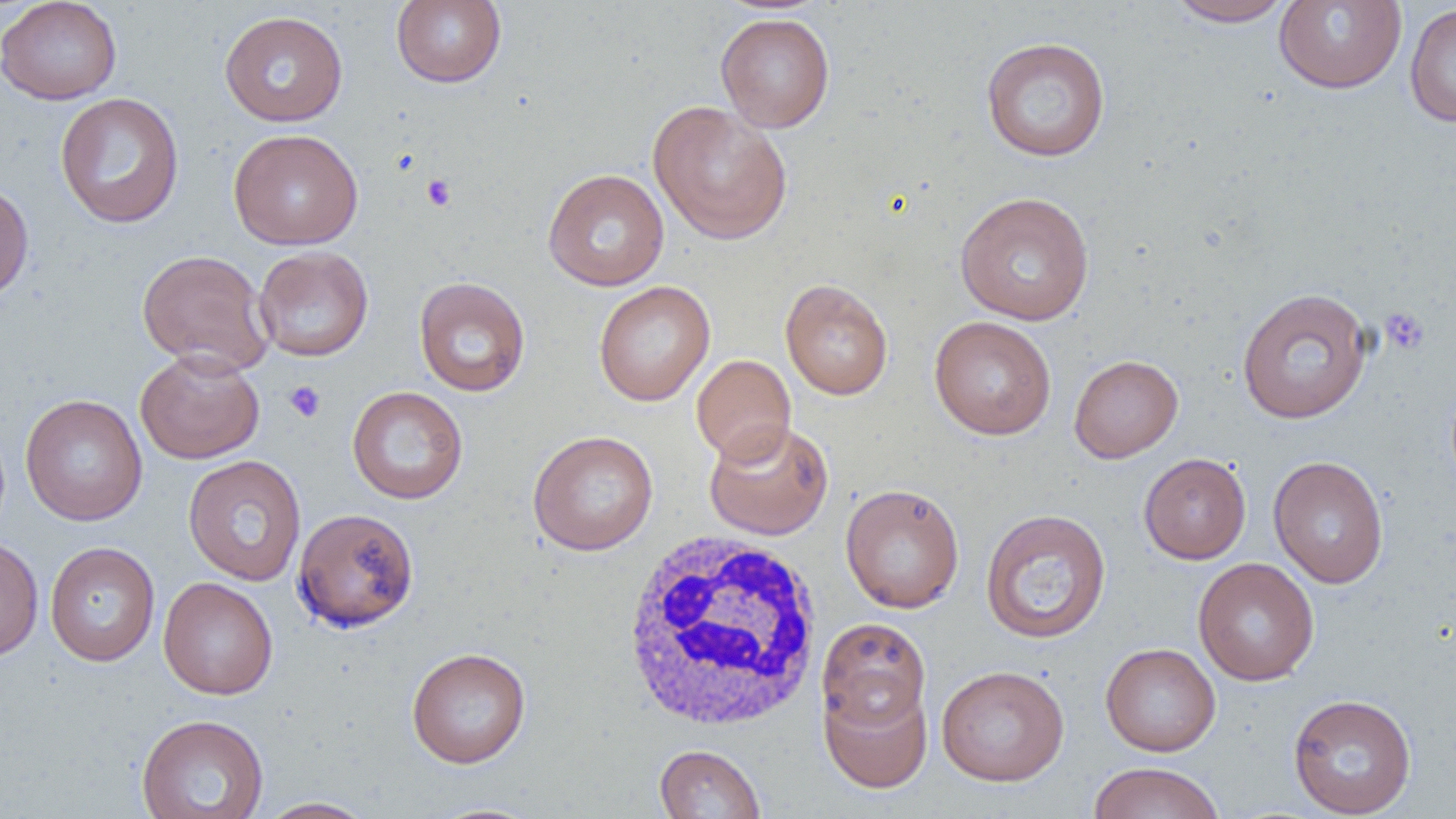
{
  "slide_level_diagnosis": "no evidence of blood parasites",
  "magnification": "1000x",
  "white_blood_cell_locations": "approximate bounding boxes as [x1, y1, x2, y2] in pixels: [618, 531, 824, 733]",
  "field_of_view": "one of a larger specimen",
  "uninfected_red_blood_cell_locations": "approximate bounding boxes as [x1, y1, x2, y2] in pixels: [0, 0, 122, 105], [391, 0, 507, 88], [1166, 0, 1295, 27], [1273, 0, 1407, 94], [1404, 4, 1456, 127], [219, 10, 349, 127], [715, 12, 836, 133], [980, 36, 1111, 162], [54, 92, 185, 228], [647, 101, 794, 246], [228, 128, 364, 251], [542, 168, 670, 291], [0, 179, 34, 306], [954, 191, 1095, 325], [252, 246, 373, 362], [136, 249, 274, 375], [414, 276, 530, 397], [779, 278, 894, 400], [593, 281, 715, 406], [1236, 287, 1373, 424], [929, 315, 1057, 440], [134, 348, 265, 464], [691, 354, 796, 464], [1069, 354, 1183, 463], [346, 386, 469, 504], [20, 394, 148, 526], [704, 419, 834, 541], [527, 430, 659, 556], [1139, 452, 1252, 564], [183, 454, 307, 586], [1268, 455, 1389, 588], [840, 483, 965, 613], [293, 508, 419, 633], [979, 508, 1112, 644], [0, 535, 44, 661], [45, 541, 161, 666], [1193, 557, 1320, 686], [158, 576, 279, 699], [816, 618, 931, 731], [1100, 642, 1221, 756], [406, 647, 531, 769], [936, 664, 1070, 786], [819, 678, 933, 793], [1288, 693, 1417, 817], [136, 713, 270, 819], [653, 744, 766, 818], [1086, 761, 1226, 819], [255, 797, 377, 818], [419, 802, 549, 818]",
  "image_size": "1456×819 pixels",
  "platelet_locations": "approximate bounding boxes as [x1, y1, x2, y2] in pixels: [422, 174, 456, 211], [1380, 307, 1430, 356], [284, 380, 326, 423]",
  "modality": "optical microscopy",
  "preparation": "thin blood film"
}